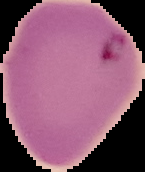
The area outside the segmented cell region is set to black. Result: Plasmodium parasites detected. From a thin blood smear. Image is 145×172 pixels.